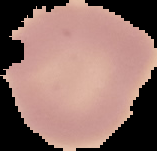
From a thin blood film. Result: no malaria parasites seen. Cell region segmented out of the field of view; the surrounding area is masked to black. Image is 157×151 pixels.